Give the extent of all Plasmodium falciparum-infected red blood cells.
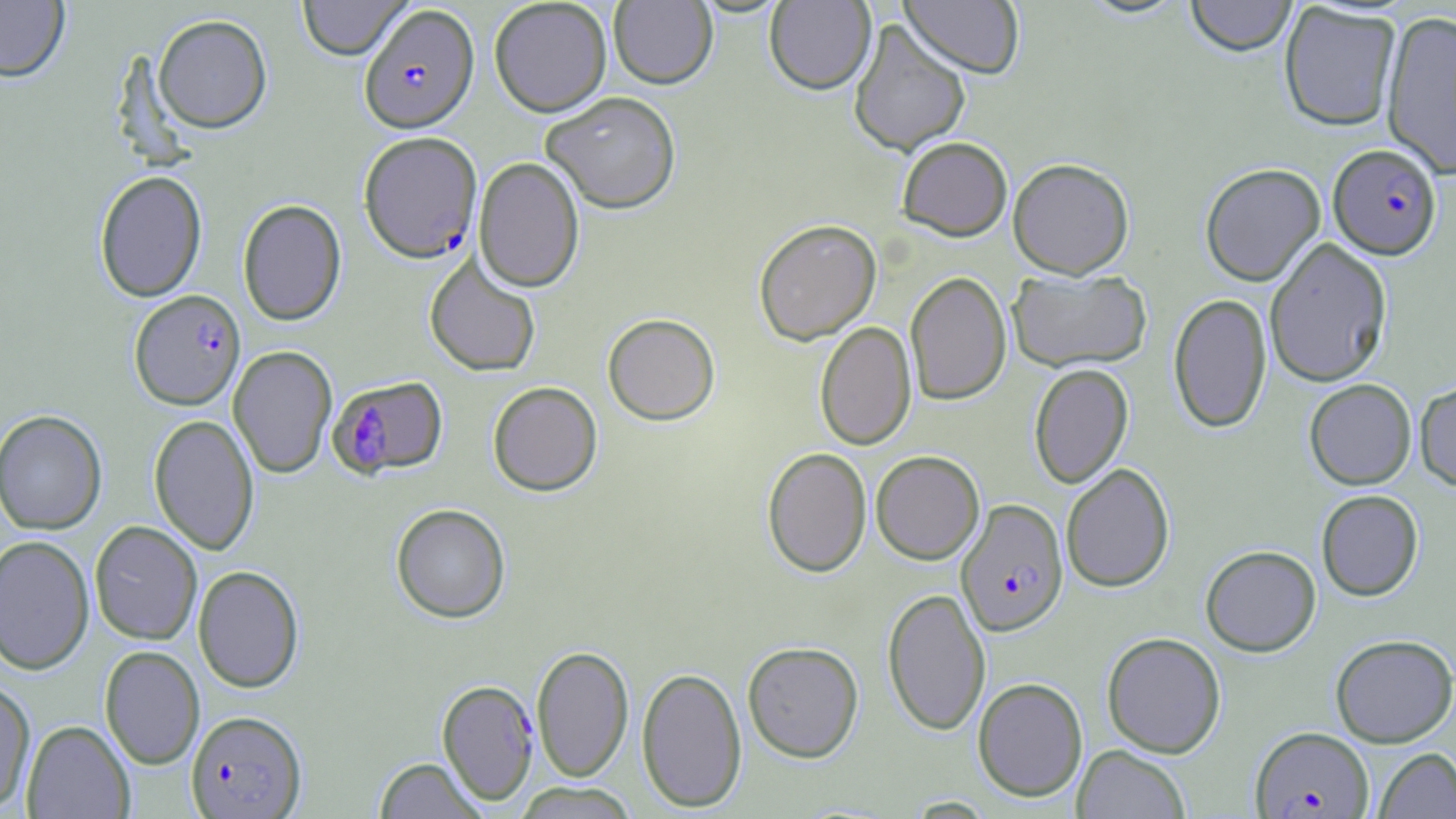
Approximate bounding boxes as (x1,y1)-(x2,y2) corner pairs in pixels.
Plasmodium falciparum-infected red blood cells: (358,4)-(479,134), (358,131)-(483,264), (1328,144)-(1442,259), (129,290)-(245,410), (328,376)-(448,479), (956,498)-(1068,636), (436,679)-(539,805), (186,710)-(307,818), (1250,727)-(1373,817).

Uninfected red blood cell locations: (297,0)-(412,60), (489,0)-(612,117), (764,0)-(876,96), (899,0)-(1024,78), (1077,0)-(1192,20), (1184,0)-(1297,56), (0,1)-(70,83), (609,1)-(718,90), (1279,3)-(1401,132), (1380,9)-(1456,178), (153,15)-(272,133), (848,18)-(972,157), (541,91)-(682,214), (897,136)-(1013,240), (473,157)-(584,293), (1008,158)-(1134,278), (1200,163)-(1325,286), (94,170)-(207,302), (237,199)-(347,326), (754,219)-(881,345), (1264,237)-(1393,388), (424,254)-(541,377), (1007,268)-(1152,373), (905,271)-(1012,406), (1168,293)-(1272,433), (603,313)-(720,426), (815,321)-(916,450), (228,346)-(337,479), (1029,363)-(1133,488), (1304,379)-(1416,489), (1414,380)-(1456,489), (487,382)-(603,496), (0,409)-(108,535), (149,414)-(259,555), (762,447)-(872,578), (871,450)-(984,564), (1061,462)-(1175,592), (1316,490)-(1423,601), (391,503)-(511,624), (89,521)-(202,645), (0,535)-(95,675), (1200,544)-(1321,656), (193,565)-(304,693), (882,587)-(990,736), (1102,632)-(1226,758), (1330,633)-(1456,747), (742,641)-(864,763), (99,645)-(204,768), (531,645)-(634,782), (636,666)-(747,812), (972,677)-(1088,802), (0,679)-(36,812), (22,720)-(135,819), (1072,744)-(1191,818), (1373,748)-(1456,818), (373,757)-(488,819), (511,782)-(640,818). Slide-level diagnosis: Plasmodium falciparum. Thin blood smear. Light microscopy. Single field of view. Image is 1456×819 pixels. May-Grünwald-Giemsa stain. Captured at 1000x magnification.